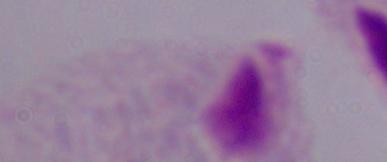
Photomicrograph. A trichomonad is seen. 1000x magnification.